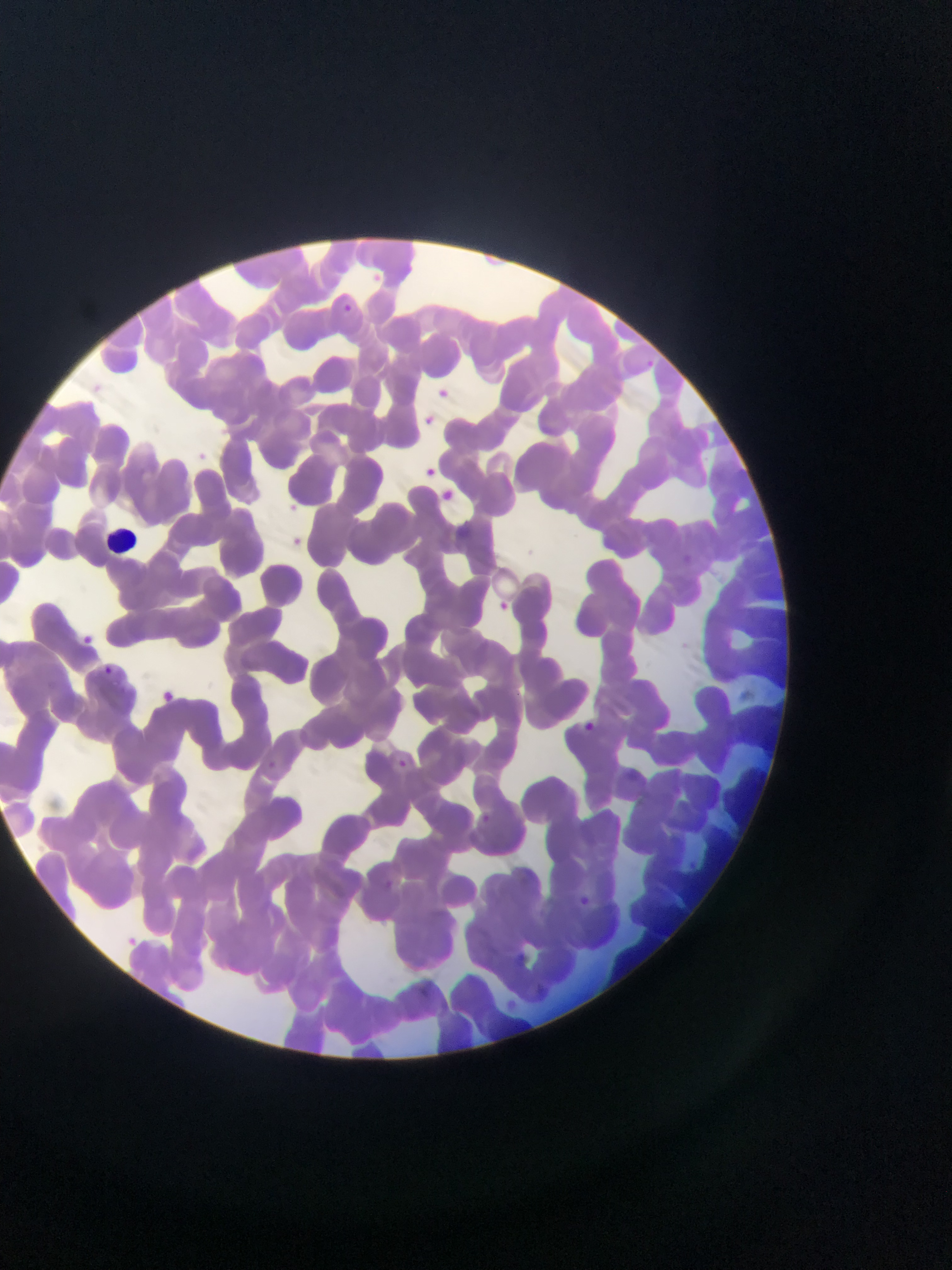
Approximate bounding boxes as {left, top, right, bottom} in pixels. Malaria parasite locations: {342, 301, 357, 314}, {646, 356, 662, 371}, {498, 597, 524, 619}, {103, 666, 113, 676}, {395, 758, 411, 772}, {265, 760, 281, 770}, {474, 809, 503, 830}, {576, 894, 597, 918}, {513, 950, 525, 962}. Leukocyte locations: {109, 520, 145, 557}. Thin blood film. One field of view. Photographed through a microscope with a mobile-phone camera. Sample from Ghana. Image is 952×1270 pixels.